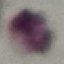 Result: no malaria parasites seen. Thin smear of blood. Acquired by smartphone through the microscope eyepiece. Automatically extracted cell patch, resized to 64 × 64 pixels. Giemsa stain.